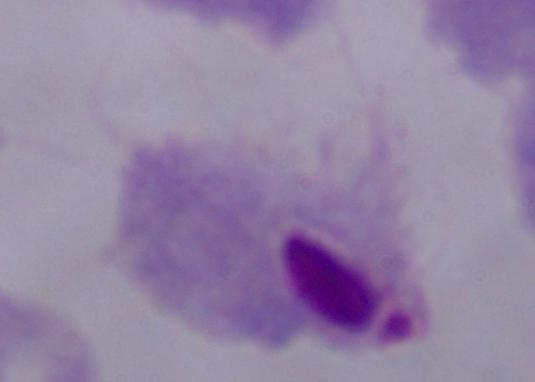 A trichomonad is shown. Captured at 1000x magnification. Micrograph.